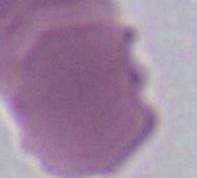 An erythrocyte is shown. Photomicrograph. Captured at 1000x magnification.